Identify the parasite.
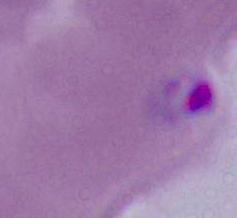

Plasmodium.

{
  "modality": "micrograph",
  "magnification": "400x or 1000x"
}